Give the position of every leukocyte visible.
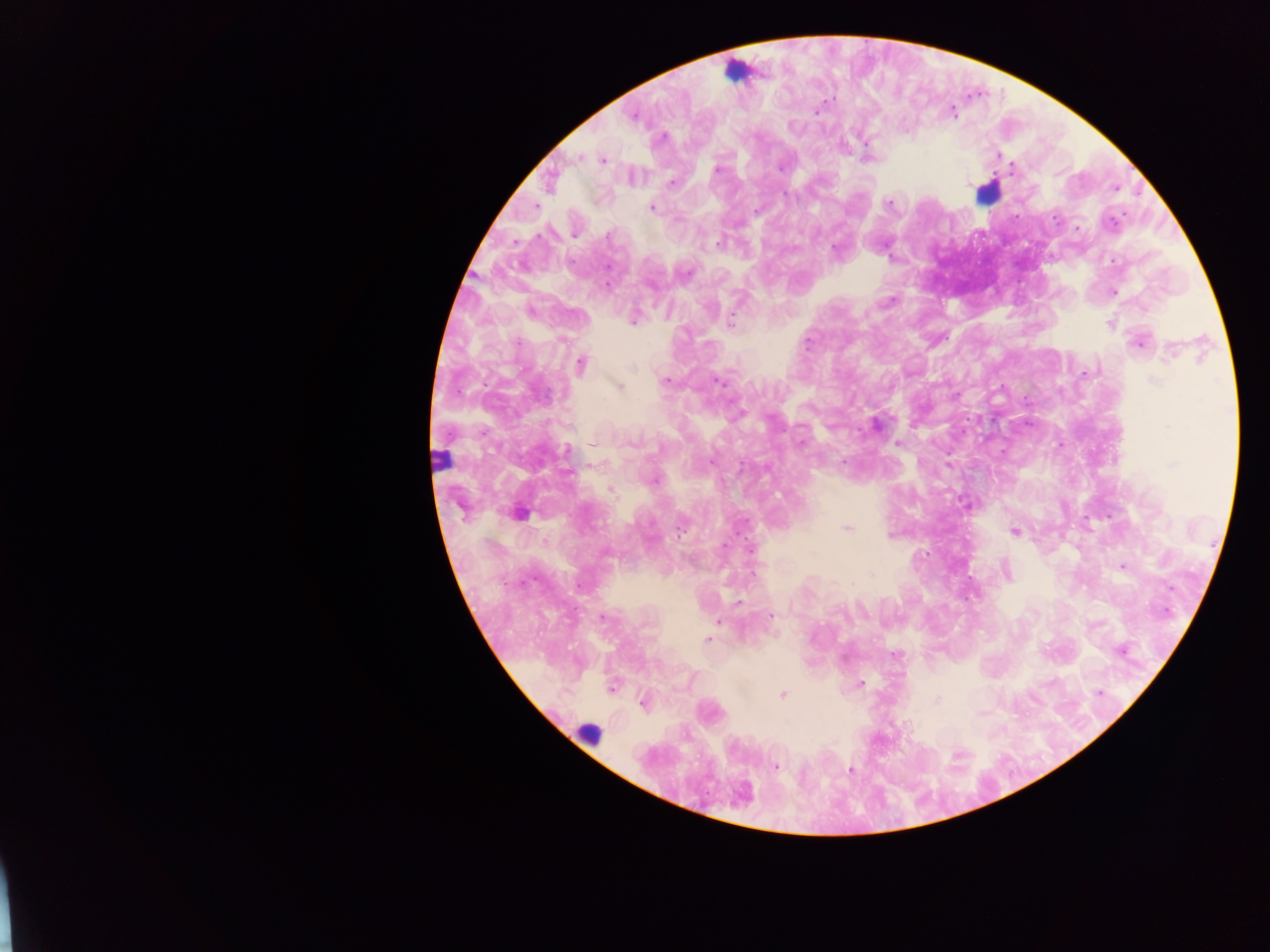
Approximate centers as (x, y) in pixels.
Leukocytes: (735, 71), (986, 191), (440, 460), (586, 734).

Malaria parasite locations: (816, 109), (632, 115), (868, 158), (603, 159), (781, 166), (716, 170), (672, 182), (1115, 187), (889, 203), (535, 206), (651, 207), (1077, 227), (574, 233), (719, 243), (1113, 291), (633, 318), (731, 324), (1110, 324), (1140, 341), (579, 365), (718, 380), (664, 381), (618, 386), (875, 424), (897, 443), (567, 451), (712, 462), (949, 463), (652, 480), (610, 489), (968, 505), (518, 513), (847, 527), (1015, 531), (749, 548), (1122, 566), (1005, 571), (738, 602), (602, 616), (770, 616), (718, 620), (708, 639), (1121, 650), (895, 655), (860, 684), (611, 687), (1099, 692), (782, 694), (644, 702), (775, 766), (851, 770). Image is 1270×952 pixels. Collected in Ghana. Thick blood film. Photographed through a microscope with a mobile-phone camera. Single field of view.